Locate and identify every blood parasite.
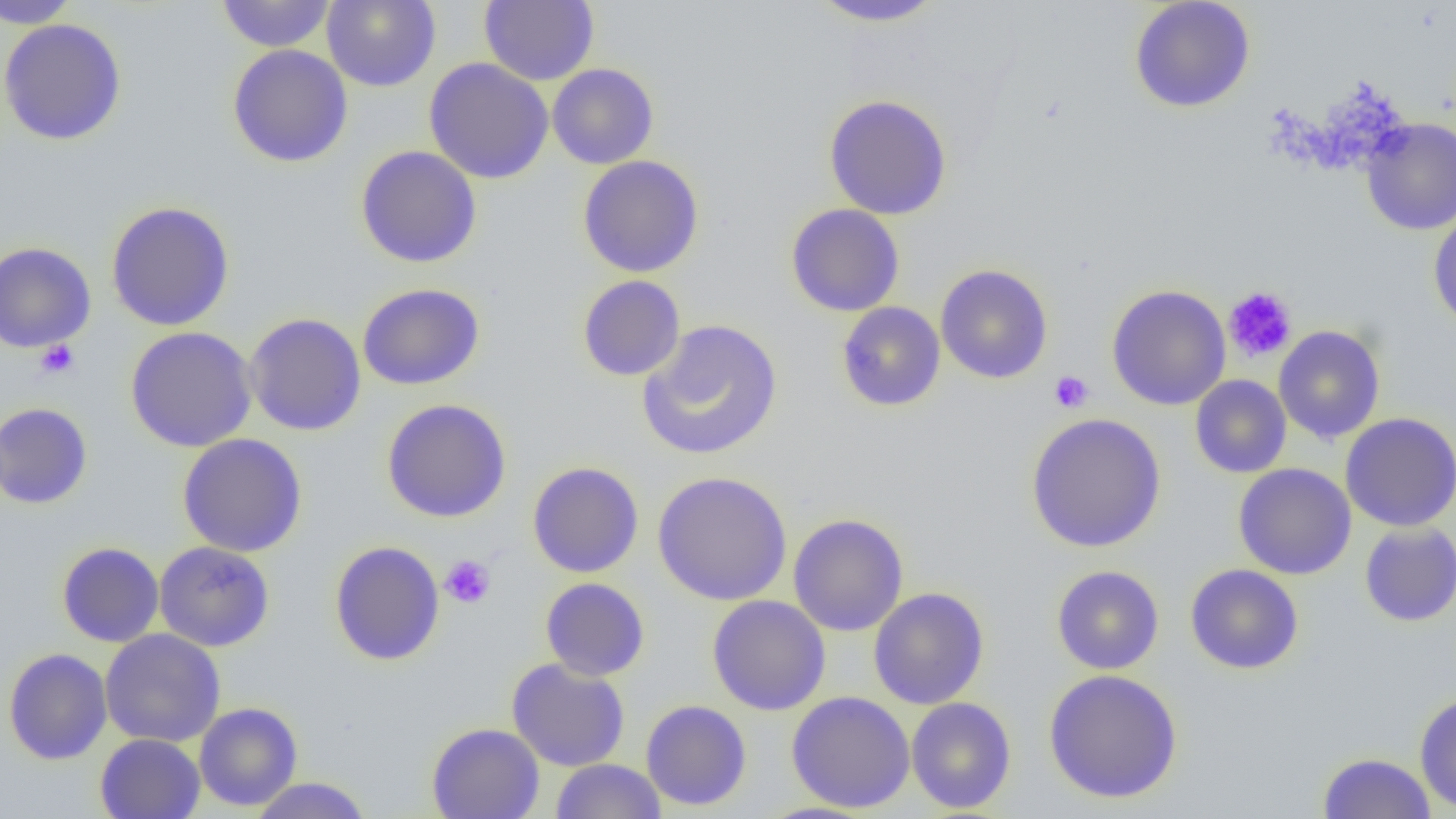

No blood parasites seen.

Approximate bounding boxes as named x1/y1/x2/y2 corners in pixels. Uninfected red blood cell locations: (x1=0, y1=0, x2=81, y2=29), (x1=215, y1=0, x2=337, y2=52), (x1=322, y1=0, x2=441, y2=91), (x1=480, y1=0, x2=599, y2=85), (x1=808, y1=0, x2=947, y2=27), (x1=1129, y1=0, x2=1256, y2=113), (x1=0, y1=18, x2=127, y2=145), (x1=227, y1=44, x2=353, y2=168), (x1=424, y1=57, x2=554, y2=184), (x1=547, y1=63, x2=659, y2=169), (x1=823, y1=94, x2=953, y2=220), (x1=1361, y1=118, x2=1456, y2=235), (x1=355, y1=145, x2=483, y2=268), (x1=577, y1=155, x2=705, y2=278), (x1=106, y1=201, x2=235, y2=331), (x1=786, y1=204, x2=905, y2=317), (x1=1428, y1=207, x2=1456, y2=331), (x1=0, y1=241, x2=96, y2=353), (x1=935, y1=264, x2=1053, y2=384), (x1=577, y1=275, x2=686, y2=381), (x1=357, y1=283, x2=485, y2=390), (x1=1106, y1=284, x2=1231, y2=410), (x1=836, y1=302, x2=946, y2=412), (x1=244, y1=312, x2=367, y2=436), (x1=638, y1=319, x2=783, y2=460), (x1=124, y1=325, x2=257, y2=452), (x1=1273, y1=325, x2=1386, y2=444), (x1=1190, y1=375, x2=1292, y2=478), (x1=381, y1=398, x2=512, y2=523), (x1=0, y1=402, x2=93, y2=509), (x1=1026, y1=412, x2=1166, y2=553), (x1=1340, y1=412, x2=1456, y2=532), (x1=177, y1=433, x2=308, y2=558), (x1=527, y1=461, x2=644, y2=578), (x1=1233, y1=463, x2=1357, y2=579), (x1=652, y1=470, x2=792, y2=606), (x1=788, y1=513, x2=908, y2=636), (x1=1359, y1=522, x2=1456, y2=627), (x1=56, y1=541, x2=164, y2=648), (x1=154, y1=541, x2=275, y2=651), (x1=329, y1=541, x2=445, y2=666), (x1=1186, y1=564, x2=1304, y2=674), (x1=1051, y1=565, x2=1164, y2=674), (x1=540, y1=577, x2=650, y2=681), (x1=868, y1=587, x2=989, y2=709), (x1=706, y1=595, x2=831, y2=715), (x1=100, y1=628, x2=226, y2=747), (x1=3, y1=648, x2=112, y2=764), (x1=506, y1=657, x2=630, y2=771), (x1=1043, y1=668, x2=1183, y2=803), (x1=786, y1=691, x2=916, y2=813), (x1=1414, y1=692, x2=1456, y2=813), (x1=906, y1=697, x2=1016, y2=813), (x1=640, y1=700, x2=752, y2=811), (x1=194, y1=702, x2=302, y2=811), (x1=427, y1=723, x2=544, y2=819), (x1=95, y1=733, x2=206, y2=819), (x1=1318, y1=752, x2=1436, y2=818), (x1=550, y1=759, x2=667, y2=819), (x1=248, y1=777, x2=373, y2=818). Platelet locations: (x1=1222, y1=286, x2=1297, y2=363), (x1=35, y1=340, x2=80, y2=380), (x1=1049, y1=370, x2=1094, y2=413), (x1=440, y1=555, x2=495, y2=609). Slide-level diagnosis: negative for blood parasites. Optical microscopy. One field of a larger specimen. Image is 1456×819 pixels. Thin blood film. Captured at 1000x magnification.